Classify this cell by malaria status.
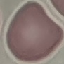
It is uninfected.

image type = cell patch, automatically extracted from a larger field of view and resized to 64 × 64 pixels
capture = smartphone camera at the microscope eyepiece
preparation = thin blood film
stain = Giemsa